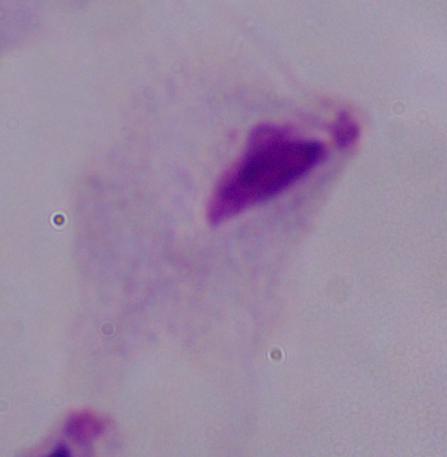
modality: micrograph
magnification: 1000x
identification: trichomonad